Assess the morphology of the erythrocytes.
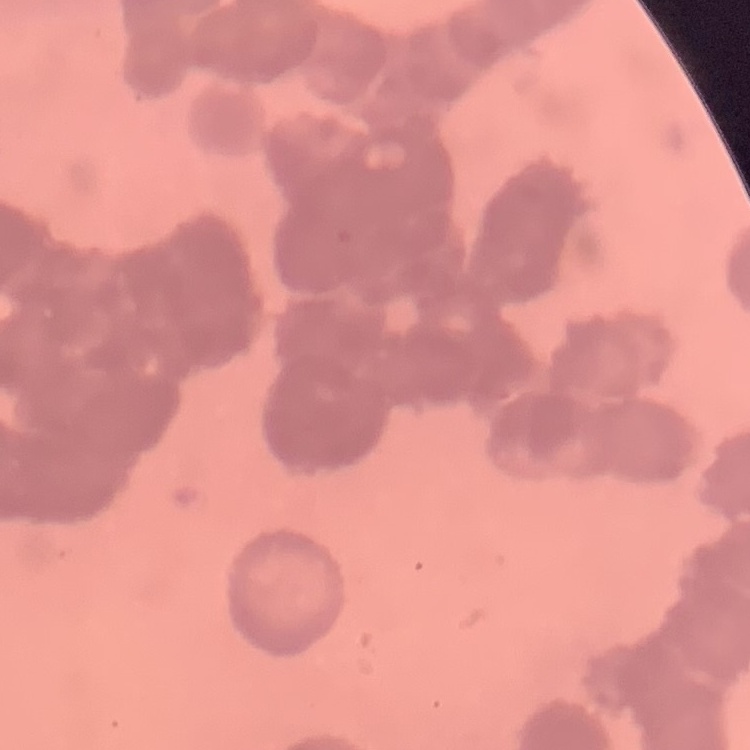
They show rouleaux formation.

stain: Field's or Giemsa
preparation: thin blood smear
image_type: square crop of a larger photomicrograph